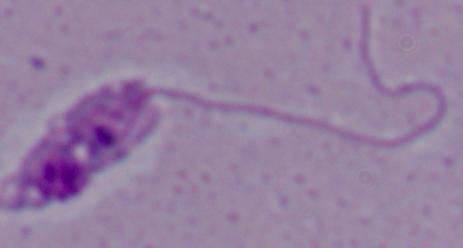
Summary:
  - Identification: Leishmania
  - Magnification: 1000x
  - Modality: micrograph